Locate every white blood cell.
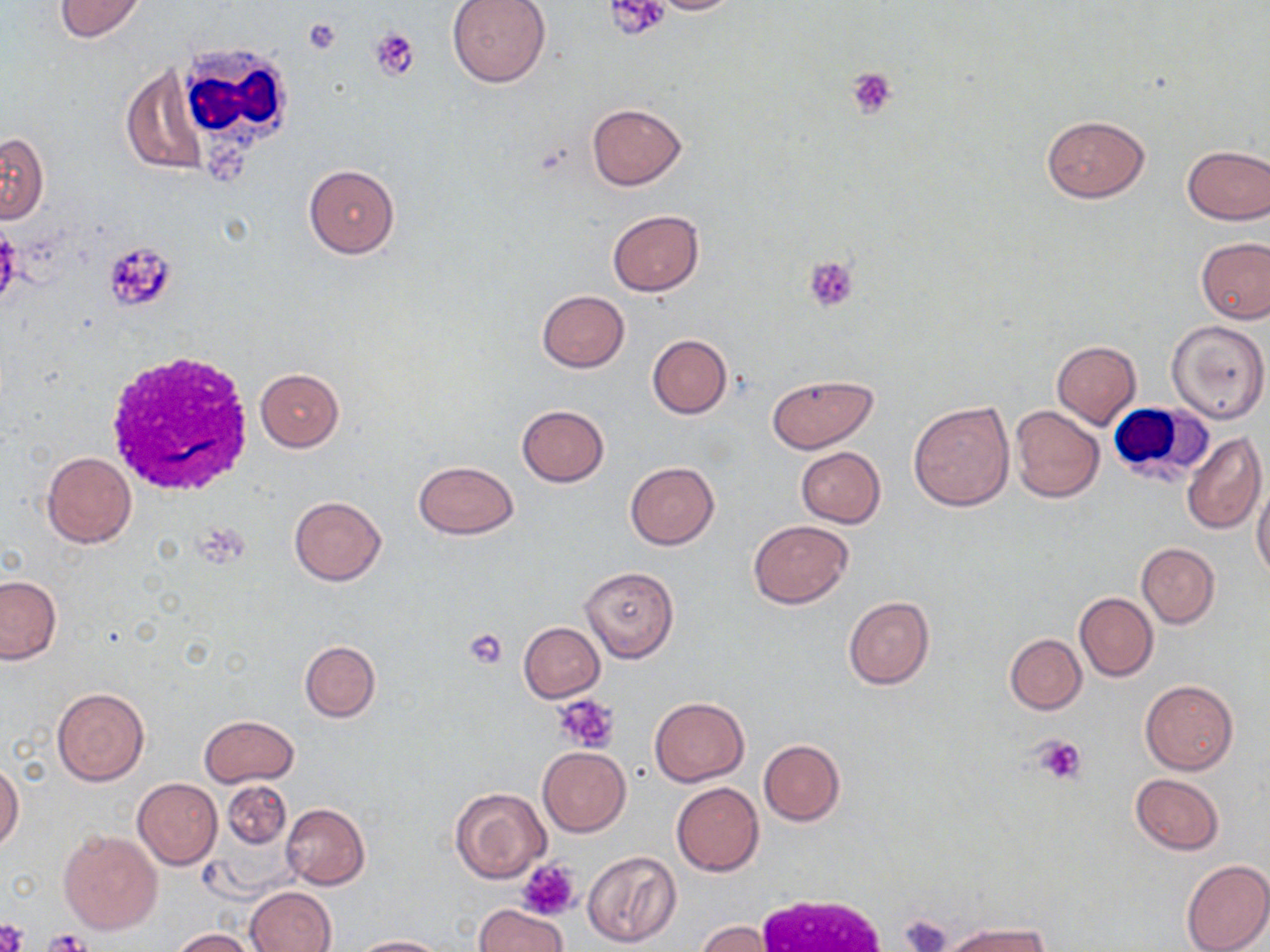
Approximate bounding boxes as named x1/y1/x2/y2 corners in pixels.
White blood cells: (x1=170, y1=43, x2=298, y2=152), (x1=102, y1=352, x2=253, y2=496), (x1=1109, y1=405, x2=1214, y2=485), (x1=749, y1=893, x2=892, y2=952).

Uninfected red blood cell locations: (x1=53, y1=0, x2=148, y2=40), (x1=446, y1=0, x2=551, y2=87), (x1=639, y1=0, x2=746, y2=15), (x1=122, y1=68, x2=206, y2=175), (x1=587, y1=103, x2=687, y2=191), (x1=1041, y1=114, x2=1150, y2=202), (x1=1, y1=132, x2=48, y2=223), (x1=1180, y1=145, x2=1270, y2=224), (x1=303, y1=164, x2=400, y2=258), (x1=607, y1=210, x2=704, y2=296), (x1=1195, y1=237, x2=1269, y2=324), (x1=536, y1=290, x2=630, y2=372), (x1=1167, y1=319, x2=1269, y2=424), (x1=646, y1=334, x2=732, y2=419), (x1=1051, y1=340, x2=1141, y2=428), (x1=255, y1=368, x2=344, y2=451), (x1=764, y1=375, x2=878, y2=453), (x1=908, y1=401, x2=1015, y2=510), (x1=517, y1=405, x2=609, y2=486), (x1=1010, y1=405, x2=1103, y2=503), (x1=1182, y1=431, x2=1266, y2=534), (x1=796, y1=447, x2=885, y2=528), (x1=42, y1=451, x2=136, y2=548), (x1=413, y1=459, x2=519, y2=540), (x1=625, y1=462, x2=719, y2=549), (x1=1252, y1=478, x2=1270, y2=581), (x1=288, y1=496, x2=386, y2=585), (x1=747, y1=519, x2=853, y2=608), (x1=1137, y1=542, x2=1219, y2=627), (x1=581, y1=566, x2=679, y2=661), (x1=0, y1=575, x2=61, y2=664), (x1=1075, y1=592, x2=1157, y2=682), (x1=843, y1=596, x2=934, y2=689), (x1=518, y1=622, x2=604, y2=702), (x1=1005, y1=633, x2=1086, y2=714), (x1=299, y1=640, x2=381, y2=722), (x1=1140, y1=680, x2=1238, y2=775), (x1=51, y1=686, x2=149, y2=786), (x1=650, y1=697, x2=749, y2=786), (x1=198, y1=715, x2=300, y2=787), (x1=758, y1=739, x2=845, y2=826), (x1=537, y1=748, x2=630, y2=836), (x1=0, y1=762, x2=23, y2=851), (x1=1130, y1=774, x2=1224, y2=855), (x1=134, y1=779, x2=222, y2=868), (x1=222, y1=781, x2=291, y2=848), (x1=672, y1=782, x2=764, y2=876), (x1=450, y1=787, x2=551, y2=884), (x1=281, y1=802, x2=369, y2=889), (x1=59, y1=831, x2=162, y2=934), (x1=580, y1=850, x2=681, y2=949), (x1=1180, y1=858, x2=1270, y2=952), (x1=246, y1=887, x2=335, y2=952), (x1=475, y1=903, x2=567, y2=952), (x1=941, y1=920, x2=1047, y2=952), (x1=697, y1=921, x2=773, y2=952), (x1=169, y1=928, x2=257, y2=951), (x1=353, y1=936, x2=447, y2=952). Platelet locations: (x1=605, y1=0, x2=671, y2=41), (x1=304, y1=18, x2=342, y2=55), (x1=369, y1=27, x2=419, y2=79), (x1=846, y1=66, x2=899, y2=119), (x1=102, y1=241, x2=176, y2=312), (x1=803, y1=256, x2=858, y2=312), (x1=463, y1=627, x2=509, y2=669), (x1=555, y1=696, x2=621, y2=753), (x1=1032, y1=734, x2=1087, y2=785), (x1=517, y1=859, x2=582, y2=920), (x1=900, y1=913, x2=950, y2=952), (x1=0, y1=919, x2=28, y2=952), (x1=45, y1=929, x2=89, y2=952). Slide-level diagnosis: negative for blood parasites. Captured at 1000x magnification. One field of a larger specimen. May-Grünwald-Giemsa-stained preparation. Light microscopy. Thin blood film. Image is 1270×952 pixels.